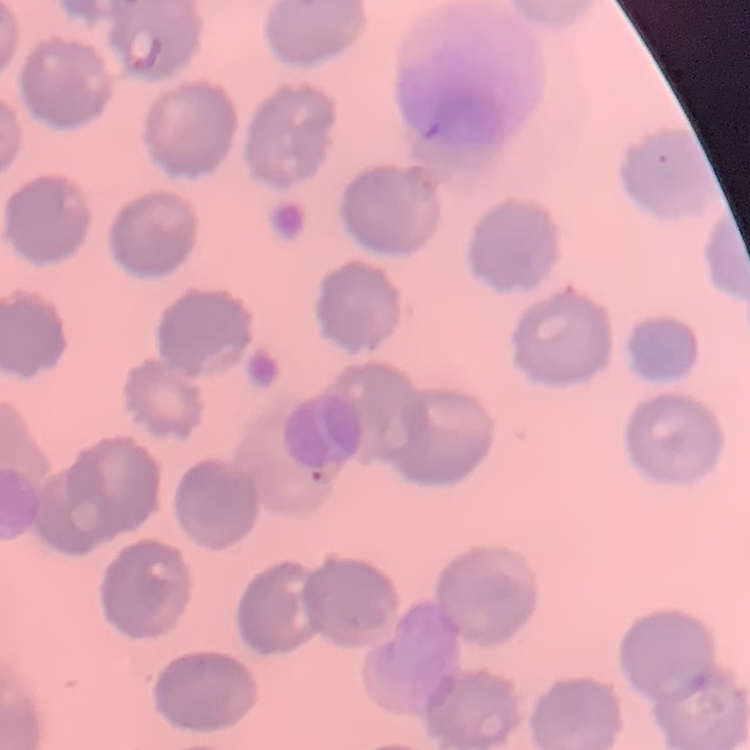
The red blood cells exhibit no rouleaux formation. Field's or Giemsa stain. Thin blood film. One tile cut from a larger photomicrograph.